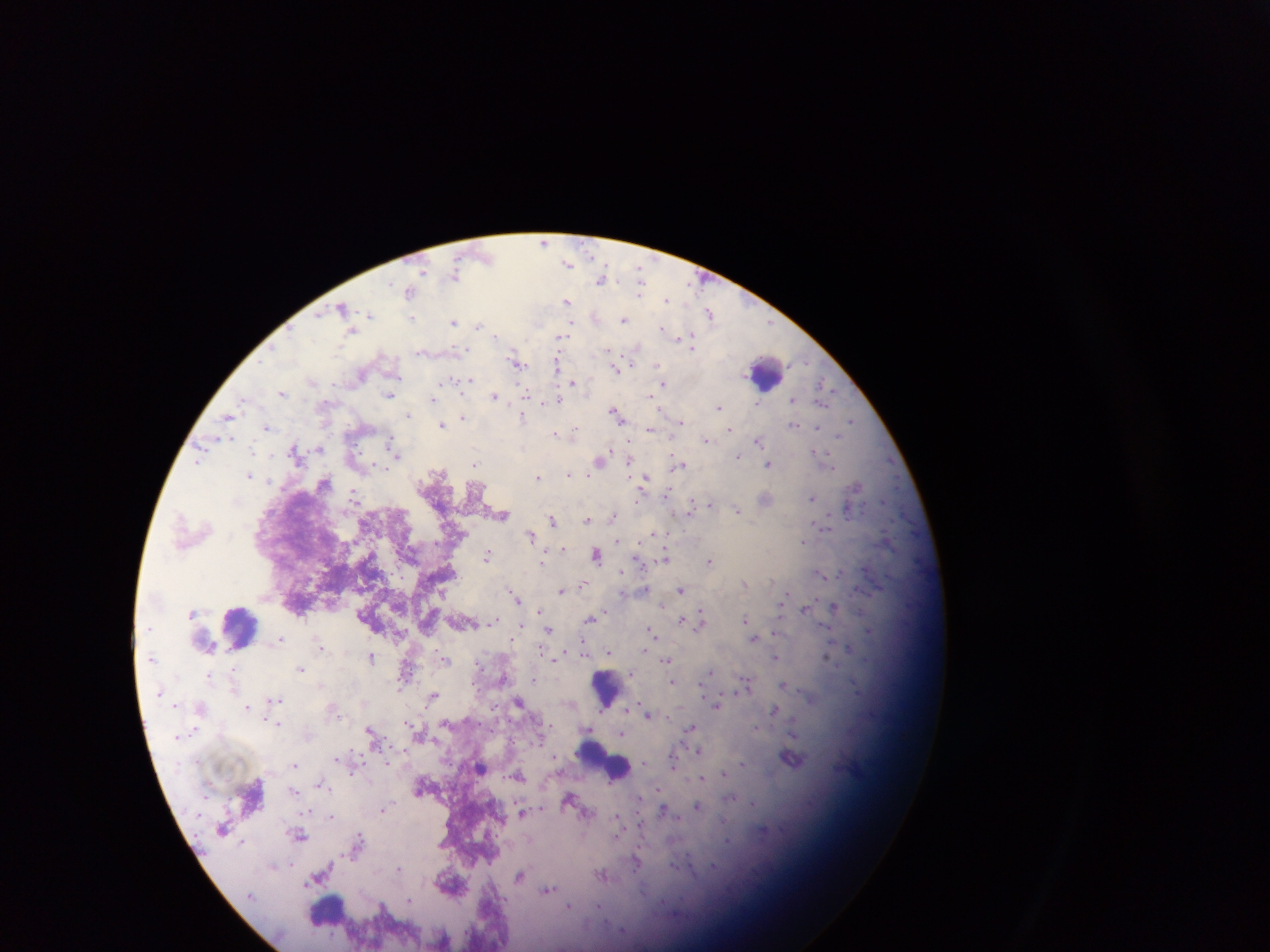

Approximate centers as (x, y) in pixels. Malaria parasite locations: (544, 240), (568, 265), (423, 271), (455, 277), (452, 281), (601, 281), (639, 281), (390, 283), (641, 288), (408, 290), (665, 299), (567, 301), (342, 307), (709, 312), (369, 314), (413, 320), (623, 320), (454, 322), (572, 322), (481, 326), (661, 329), (351, 331), (690, 336), (496, 337), (677, 337), (559, 339), (694, 341), (455, 349), (694, 349), (606, 350), (637, 350), (558, 361), (516, 363), (804, 363), (655, 366), (557, 367), (614, 370), (451, 377), (446, 381), (573, 381), (820, 384), (662, 385), (825, 386), (660, 388), (282, 392), (390, 394), (525, 394), (494, 397), (557, 399), (793, 400), (433, 401), (825, 404), (719, 406), (613, 410), (408, 415), (228, 416), (464, 416), (521, 417), (850, 420), (681, 423), (266, 425), (440, 425), (793, 426), (819, 426), (574, 429), (649, 430), (730, 432), (553, 433), (706, 438), (839, 438), (231, 439), (758, 441), (612, 446), (251, 448), (294, 448), (318, 448), (814, 451), (396, 452), (817, 453), (739, 456), (630, 459), (597, 461), (197, 462), (682, 464), (474, 465), (768, 465), (443, 473), (567, 473), (247, 475), (536, 477), (269, 482), (857, 485), (355, 492), (639, 497), (813, 497), (885, 501), (710, 502), (691, 508), (738, 510), (846, 510), (504, 517), (612, 517), (551, 520), (589, 520), (825, 528), (530, 535), (805, 541), (563, 550), (597, 554), (488, 557), (665, 557), (637, 560), (543, 561), (710, 561), (542, 564), (863, 569), (623, 572), (819, 574), (581, 584), (560, 590), (512, 591), (681, 591), (559, 593), (443, 595), (514, 596), (785, 597), (517, 602), (834, 607), (538, 610), (804, 610), (780, 611), (702, 616), (591, 618), (495, 619), (680, 620), (745, 620), (522, 623), (701, 623), (825, 626), (650, 628), (549, 630), (868, 630), (774, 632), (280, 639), (756, 639), (510, 641), (321, 645), (583, 648), (847, 648), (645, 650), (607, 653), (773, 655), (370, 657), (827, 657), (556, 659), (666, 659), (445, 660), (480, 665), (302, 670), (234, 673), (711, 673), (211, 675), (534, 679), (748, 680), (671, 681), (783, 685), (400, 688), (701, 688), (234, 690), (434, 694), (278, 700), (205, 708), (248, 709), (774, 711), (647, 715), (267, 722), (445, 722), (281, 724), (411, 725), (691, 727), (369, 731), (793, 732), (622, 734), (698, 750), (338, 758), (791, 759), (387, 762), (672, 763), (645, 764), (296, 765), (743, 766), (724, 773), (702, 777), (292, 793), (640, 796), (732, 798), (752, 802), (664, 807), (697, 807), (385, 809), (305, 812), (521, 812), (330, 817), (617, 820), (301, 836), (242, 843), (636, 860), (288, 863), (273, 866), (399, 867), (603, 874), (519, 876), (311, 883), (548, 890), (409, 898), (383, 904), (569, 905), (599, 906). Photographed through a microscope with a mobile-phone camera. One field of view. Image is 1270×952 pixels. Sample from Ghana. Thick blood smear.